Locate platelets.
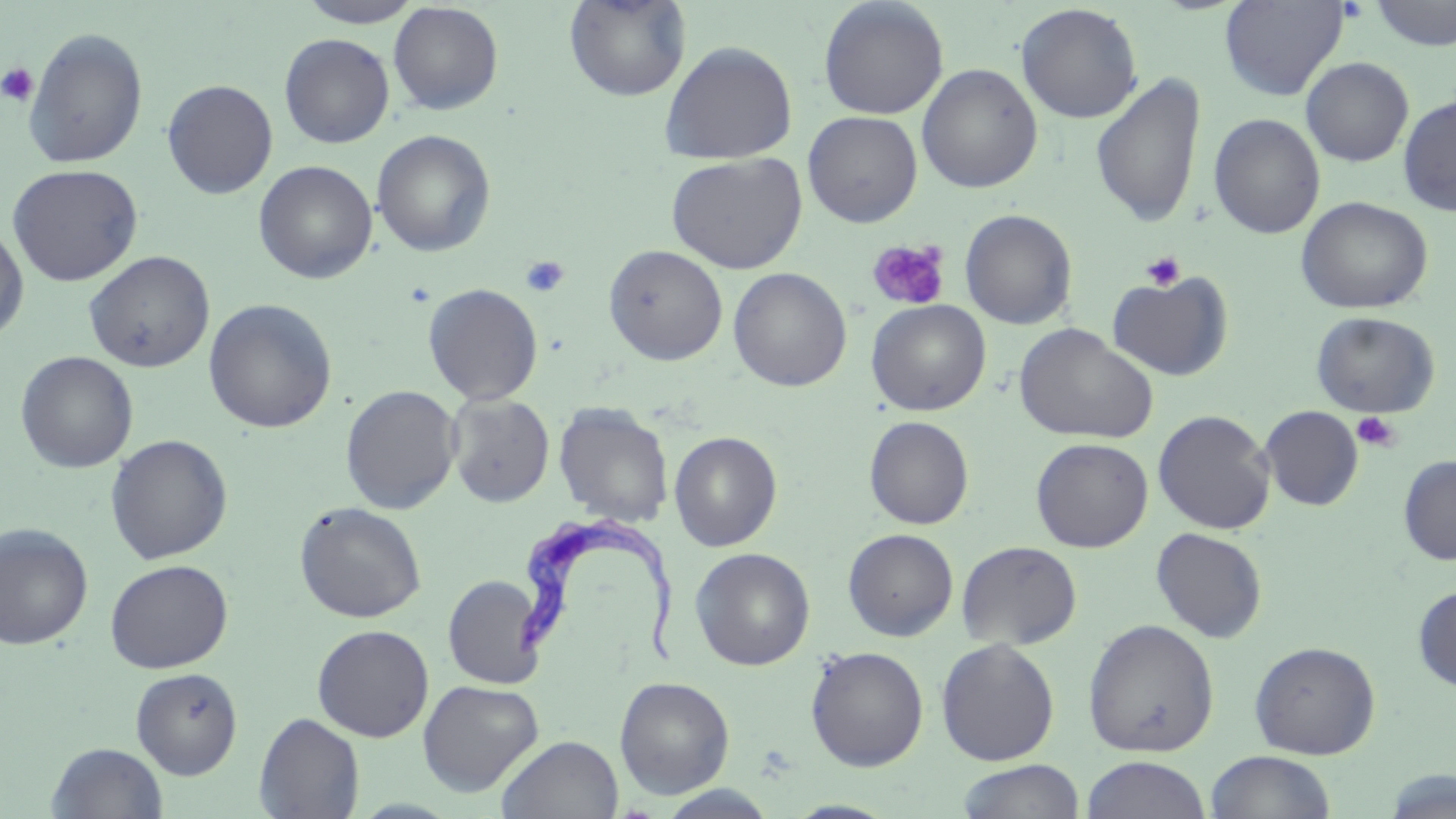
Approximate bounding boxes as [x1, y1, x2, y2] in pixels.
Platelets: [0, 62, 39, 107], [867, 238, 951, 311], [1141, 251, 1186, 291], [520, 255, 571, 297], [1352, 411, 1401, 452].

Summary:
  - Uninfected red blood cell locations: [296, 0, 427, 28], [564, 0, 691, 102], [1219, 0, 1349, 100], [818, 1, 949, 120], [1367, 1, 1456, 51], [388, 2, 504, 115], [1015, 3, 1143, 124], [23, 27, 148, 168], [279, 33, 395, 148], [660, 40, 798, 164], [1301, 57, 1414, 166], [916, 63, 1043, 194], [1090, 72, 1207, 228], [162, 79, 278, 199], [1398, 95, 1456, 216], [802, 111, 922, 227], [1208, 113, 1325, 239], [371, 129, 496, 257], [666, 153, 807, 273], [253, 160, 378, 284], [6, 163, 143, 287], [1296, 196, 1433, 314], [959, 209, 1077, 330], [0, 220, 29, 344], [604, 244, 728, 365], [84, 251, 215, 372], [728, 267, 852, 392], [1106, 270, 1234, 382], [423, 283, 544, 405], [203, 299, 338, 433], [866, 299, 991, 416], [1311, 311, 1440, 418], [1014, 324, 1158, 445], [15, 351, 138, 473], [340, 385, 462, 514], [446, 393, 555, 507], [554, 402, 674, 527], [1259, 406, 1363, 511], [1152, 410, 1276, 535], [864, 416, 974, 529], [668, 431, 782, 551], [105, 434, 233, 564], [1031, 437, 1153, 552], [1398, 454, 1456, 565], [294, 501, 427, 623], [0, 523, 94, 649], [1150, 527, 1268, 643], [843, 528, 959, 641], [956, 540, 1082, 651], [690, 547, 815, 670], [104, 559, 233, 673], [442, 575, 547, 689], [1412, 584, 1456, 693], [1082, 618, 1219, 757], [312, 624, 434, 742], [935, 638, 1060, 766], [1249, 640, 1381, 759], [806, 645, 929, 771], [131, 667, 243, 779], [614, 676, 735, 798], [417, 679, 543, 796], [254, 712, 365, 819], [496, 734, 624, 819], [46, 742, 169, 818], [1205, 750, 1335, 818], [1081, 755, 1211, 819], [955, 760, 1086, 818], [1381, 769, 1455, 819], [784, 799, 901, 818]
  - Trypanosoma brucei locations: [504, 511, 681, 671]
  - Slide-level diagnosis: Trypanosoma brucei
  - Magnification: 1000x
  - Modality: light microscopy
  - Stain: May-Grünwald-Giemsa
  - Image size: 1456×819 pixels
  - Field of view: one of a larger specimen
  - Preparation: thin blood film